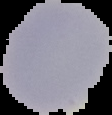
Summary:
  - Malaria status: uninfected
  - Preparation: thin blood film
  - Image type: cell region segmented out of the field of view; surrounding area masked to black
  - Image size: 112×115 pixels